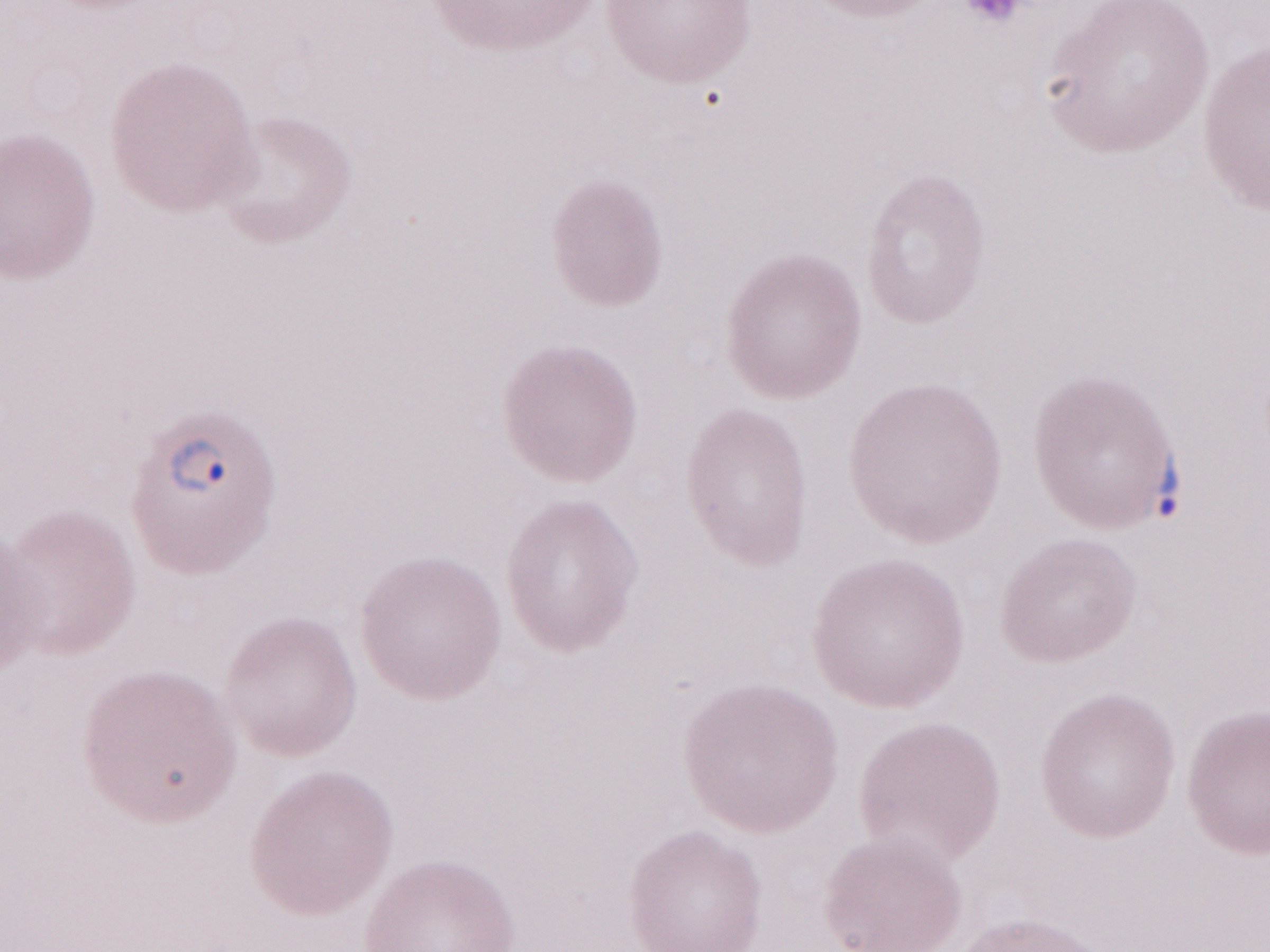
Magnification: 1,000x. Image is 1270×952 pixels. Single field of view. Olympus BX43 microscope, Olympus DP73 camera. Thin blood film. Malaria diagnosis (patient-level): positive. May-Grünwald-Giemsa-stained preparation.